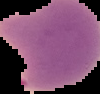
Image is 100×94 pixels. From a thin blood film. Result: Plasmodium parasites identified. Segmented cell region on a black background.